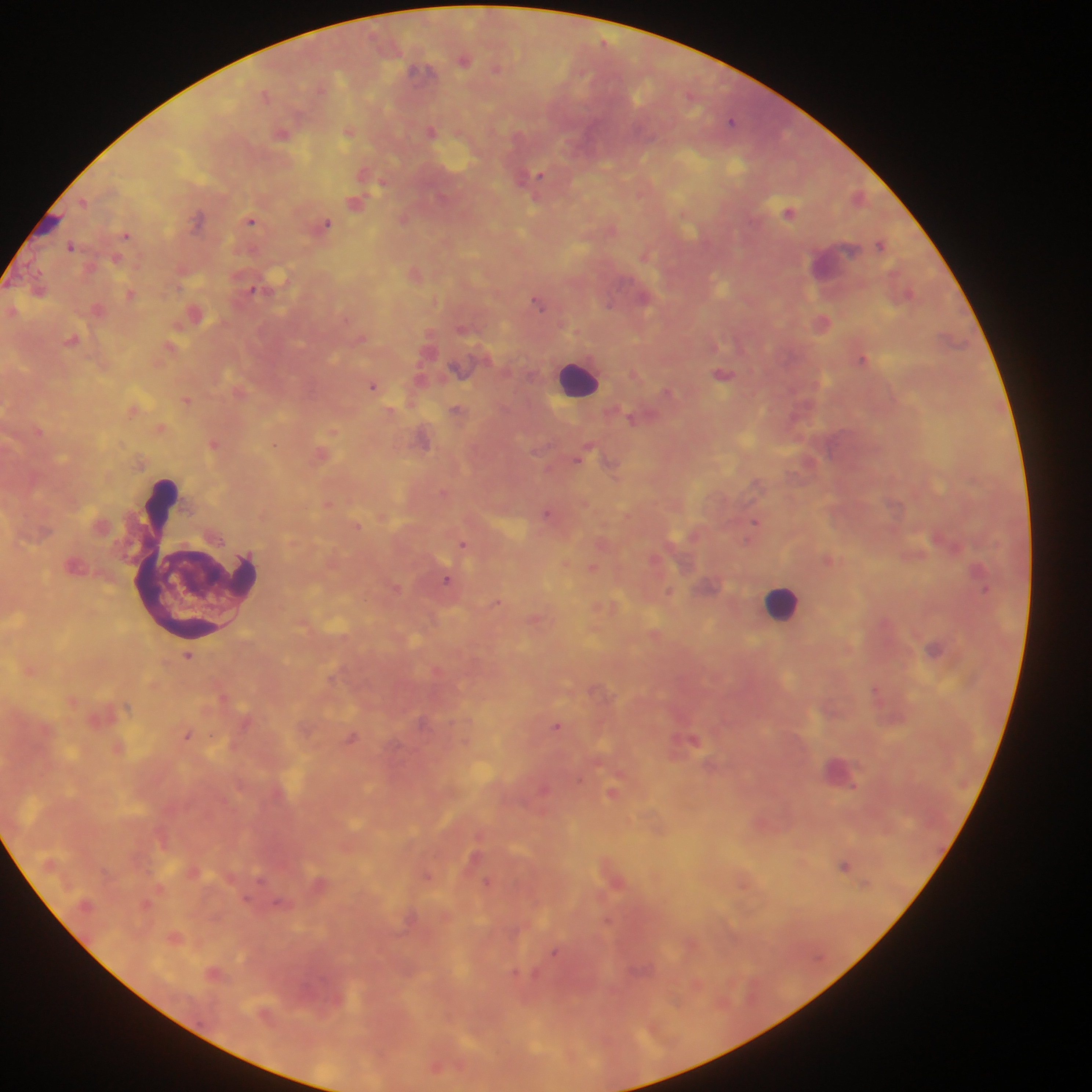
Approximate centers as [x, y] in pixels.
Summary:
  - Leukocyte locations: [578, 378], [195, 560], [781, 603]
  - Malaria parasite locations: [465, 60], [497, 68], [419, 70], [265, 94], [732, 121], [431, 131], [348, 132], [282, 134], [537, 176], [83, 201], [355, 203], [790, 212], [197, 218], [403, 219], [251, 221], [327, 224], [126, 235], [881, 244], [70, 245], [253, 288], [131, 295], [644, 297], [537, 302], [609, 305], [822, 322], [73, 340], [863, 359], [724, 374], [373, 385], [668, 392], [186, 401], [456, 408], [631, 418], [214, 444], [274, 445], [581, 457], [610, 462], [546, 513], [755, 522], [463, 544], [593, 569], [447, 580], [984, 590], [670, 591], [497, 602], [934, 648], [188, 655], [875, 689], [556, 725], [187, 736], [352, 738], [693, 740], [853, 786], [612, 793], [845, 865], [427, 876], [487, 882], [554, 952]
  - Country: Ghana
  - Preparation: thick blood smear
  - Field of view: single
  - Capture: mobile-phone photograph through a microscope
  - Image size: 1092×1092 pixels